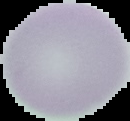

From a thin blood film. Result: negative for malaria parasites. Image is 130×121 pixels. The area outside the segmented cell region is set to black.